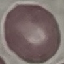

Malaria status: uninfected. Giemsa-stained preparation. Thin blood film. Cell patch, automatically extracted from a larger field of view and resized to 64 × 64 pixels. Acquired by smartphone through the microscope eyepiece.